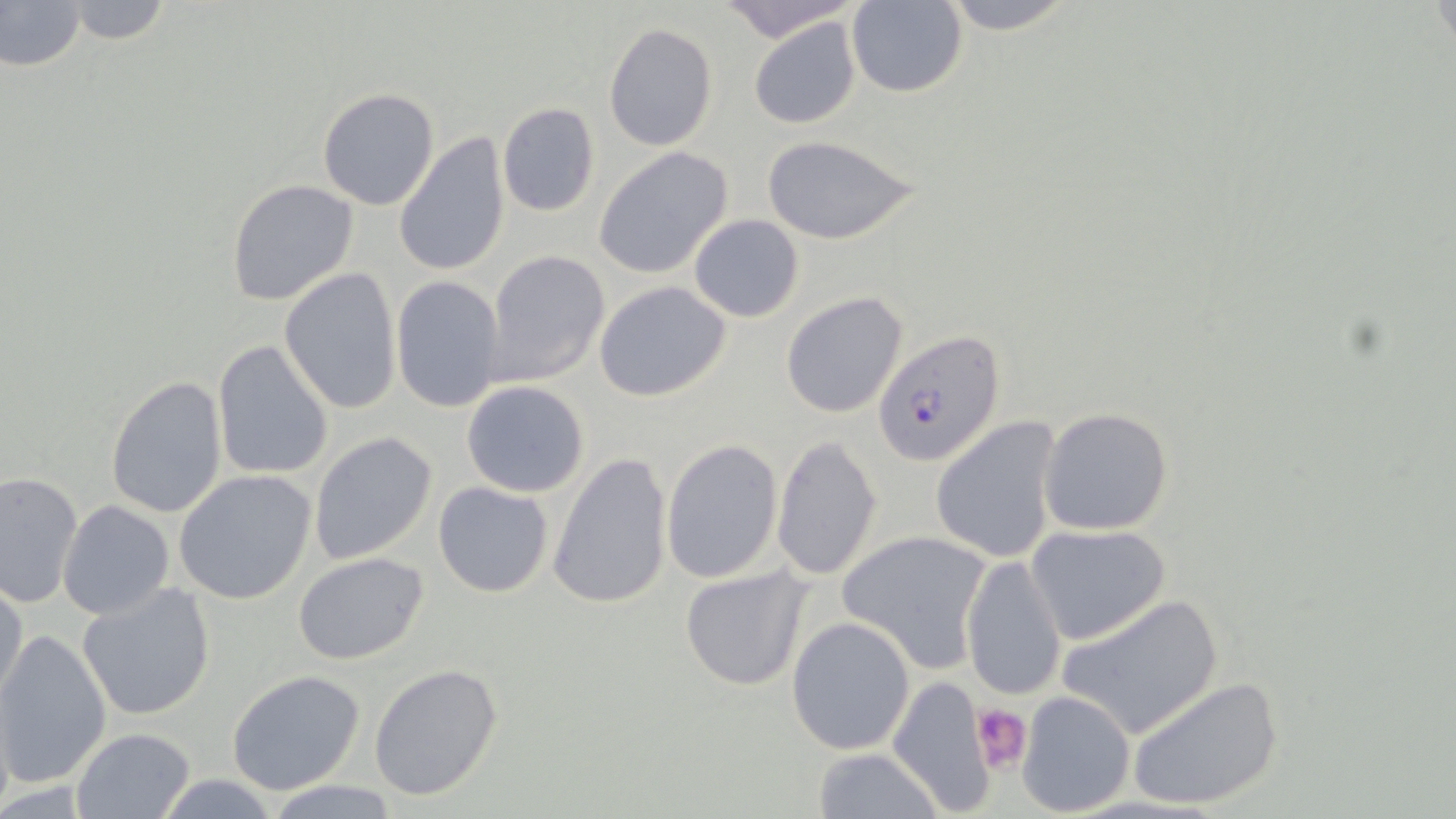
Approximate bounding boxes as (x1,y1)-(x2,y2) corner pairs in pixels. Plasmodium falciparum-infected red blood cell locations: (872,330)-(1005,468). Uninfected red blood cell locations: (721,0)-(857,43), (937,0)-(1077,35), (0,1)-(87,73), (57,1)-(175,46), (846,1)-(966,98), (747,16)-(864,130), (603,22)-(719,152), (316,88)-(440,211), (497,102)-(600,217), (394,131)-(512,278), (760,133)-(923,246), (593,147)-(734,279), (227,178)-(358,306), (689,213)-(804,321), (484,249)-(612,388), (279,267)-(402,414), (390,275)-(505,411), (594,280)-(732,402), (781,290)-(911,418), (212,340)-(334,480), (105,375)-(229,520), (461,381)-(590,498), (1038,407)-(1174,537), (931,415)-(1065,564), (309,431)-(438,565), (770,434)-(884,582), (662,439)-(782,584), (548,451)-(673,610), (174,470)-(317,605), (0,472)-(85,609), (433,480)-(555,598), (59,500)-(175,620), (1026,523)-(1173,647), (837,529)-(994,671), (293,551)-(430,666), (959,553)-(1067,704), (680,564)-(810,691), (0,576)-(27,708), (77,581)-(216,722), (1054,593)-(1224,742), (786,616)-(916,756), (0,628)-(111,792), (369,664)-(503,802), (227,669)-(367,796), (1127,674)-(1287,812), (886,676)-(998,817), (1015,691)-(1136,817), (70,728)-(194,817), (810,747)-(945,819), (266,779)-(403,817). Platelet locations: (971,703)-(1033,777). Slide-level diagnosis: Plasmodium falciparum. Captured at 1000x magnification. Thin blood smear. May-Grünwald-Giemsa stain. Single field of view. Image is 1456×819 pixels. Optical microscopy.